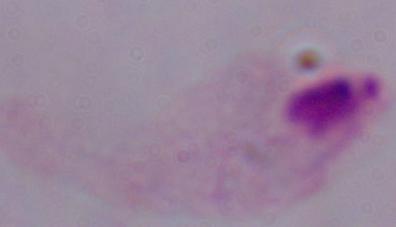

identification: trichomonad
modality: micrograph
magnification: 1000x